Describe the morphology of the erythrocytes.
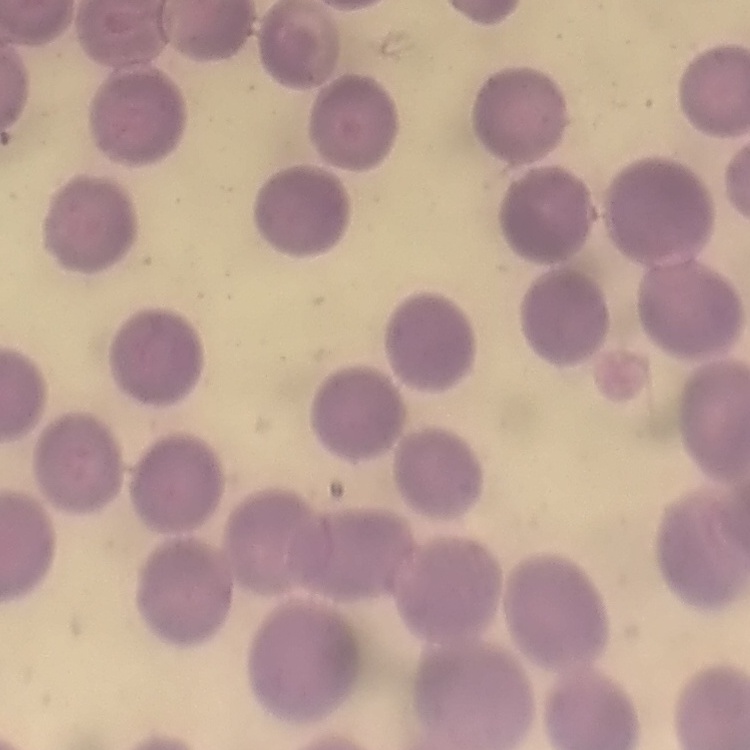
They show no rouleaux formation.

Summary:
  - Image type: one tile cut from a larger photomicrograph
  - Preparation: thin blood smear
  - Stain: Field's or Giemsa